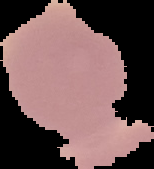
{
  "result": "no Plasmodium parasites detected",
  "image_type": "cell region segmented out of the field of view; surrounding area masked to black",
  "image_size": "154×169 pixels",
  "preparation": "thin blood film"
}